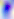

Summary:
  - Identification: Toxoplasma gondii
  - Magnification: 400x
  - Modality: micrograph